Assess this cell for malaria.
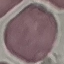
It is uninfected.

Summary:
  - Preparation: thin blood film
  - Capture: smartphone through the microscope eyepiece
  - Image type: automatically extracted cell patch, resized to 64 × 64 pixels
  - Stain: Giemsa